Assess this cell for malaria.
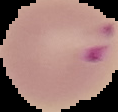

It is parasitized.

Summary:
  - Preparation: thin blood film
  - Image size: 118×112 pixels
  - Image type: segmented cell region with the area outside set to black